Report the malaria status of this cell.
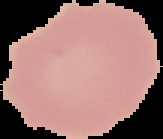

Uninfected.

Summary:
  - Image size: 163×139 pixels
  - Image type: segmented cell region on a black background
  - Preparation: thin blood film